Classify this cell by malaria status.
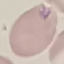

It is parasitized.

capture: smartphone through the microscope eyepiece
stain: Giemsa
image_type: automatically extracted cell patch, resized to 64 × 64 pixels
preparation: thin smear